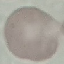

malaria_status: uninfected
image_type: cell patch, automatically extracted from a larger field of view and resized to 64 × 64 pixels
stain: Giemsa
preparation: thin blood smear
capture: smartphone through the microscope eyepiece